Outline each Plasmodium falciparum-infected red blood cell.
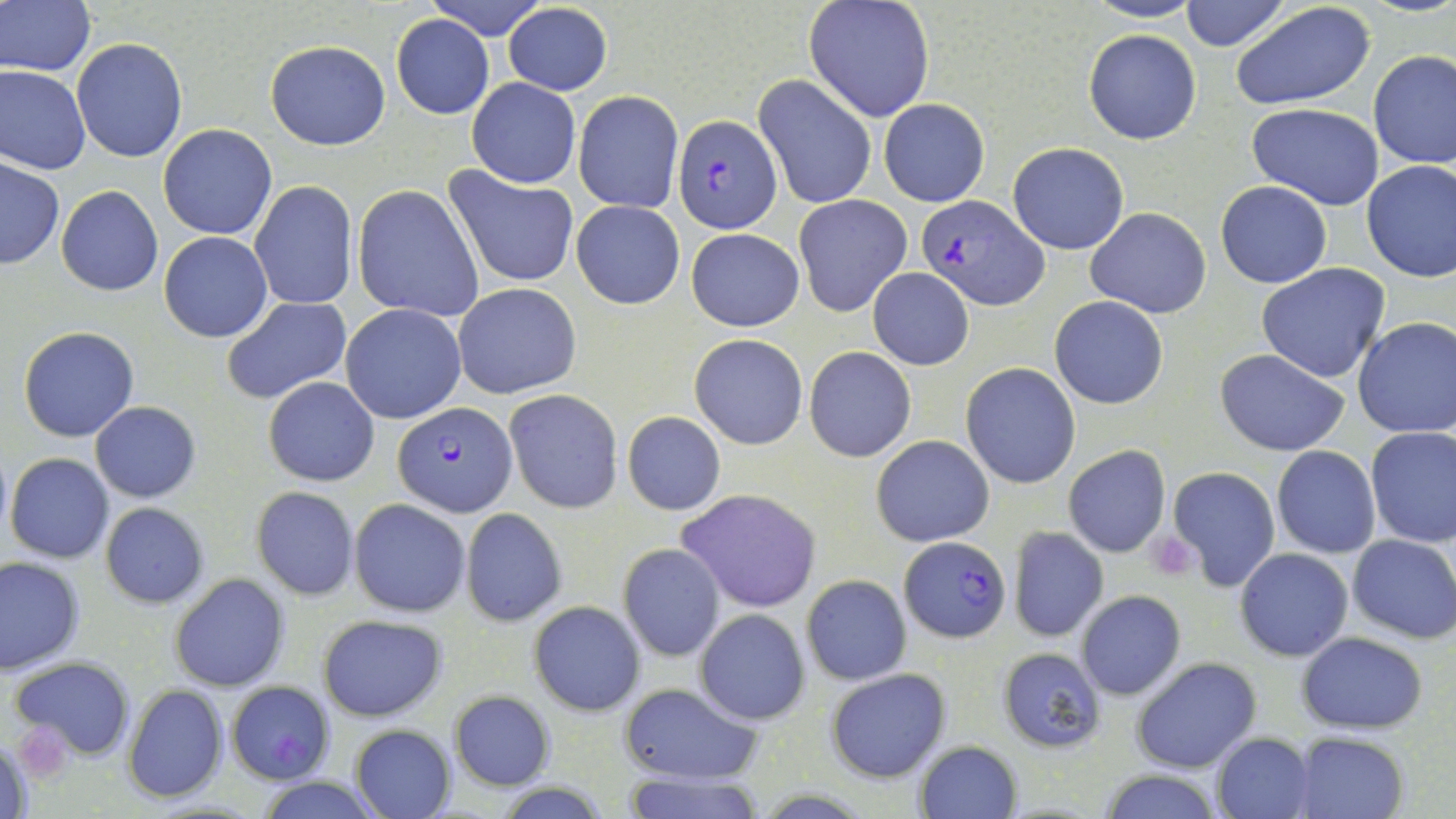
Approximate bounding boxes as [x1, y1, x2, y2] in pixels.
Plasmodium falciparum-infected red blood cells: [672, 114, 782, 233], [915, 195, 1050, 311], [392, 402, 516, 516], [897, 540, 1012, 644], [22, 725, 70, 783].

{
  "slide_level_diagnosis": "Plasmodium falciparum",
  "uninfected_red_blood_cell_locations": "approximate bounding boxes as [x1, y1, x2, y2] in pixels: [423, 0, 550, 41], [1085, 0, 1203, 24], [1181, 0, 1289, 51], [2, 1, 95, 77], [803, 1, 937, 122], [1231, 1, 1378, 110], [501, 3, 614, 95], [391, 15, 494, 120], [1084, 28, 1201, 144], [71, 37, 188, 163], [264, 40, 392, 150], [1368, 49, 1456, 169], [0, 64, 91, 175], [754, 74, 877, 208], [465, 77, 580, 189], [573, 91, 682, 213], [879, 100, 989, 206], [1247, 102, 1385, 211], [157, 124, 278, 240], [1007, 140, 1129, 254], [1, 158, 64, 269], [1360, 159, 1456, 282], [446, 166, 579, 288], [1215, 180, 1332, 288], [247, 182, 358, 309], [353, 184, 485, 322], [57, 186, 164, 296], [793, 194, 912, 316], [571, 199, 685, 310], [1085, 208, 1211, 318], [686, 227, 804, 332], [158, 231, 273, 342], [1256, 263, 1391, 384], [867, 268, 975, 371], [452, 282, 581, 400], [1050, 295, 1168, 410], [221, 296, 352, 404], [340, 303, 467, 424], [1352, 316, 1456, 438], [18, 327, 139, 443], [689, 333, 809, 451], [803, 347, 917, 462], [1214, 348, 1352, 457], [960, 363, 1081, 489], [263, 376, 381, 487], [504, 389, 623, 513], [91, 401, 201, 502], [622, 411, 726, 516], [1364, 427, 1456, 548], [871, 434, 994, 547], [1062, 444, 1171, 559], [1272, 445, 1381, 559], [5, 453, 115, 564], [1167, 466, 1280, 591], [252, 486, 359, 601], [676, 489, 823, 612], [349, 499, 470, 616], [99, 503, 209, 608], [459, 507, 567, 628], [1009, 526, 1108, 642], [1346, 534, 1456, 644], [617, 542, 727, 662], [1235, 548, 1354, 661], [0, 556, 84, 674], [170, 574, 289, 692], [801, 574, 911, 684], [1075, 590, 1186, 701], [529, 600, 645, 715], [695, 608, 810, 724], [318, 613, 447, 721], [1298, 631, 1429, 735], [996, 646, 1107, 753], [10, 656, 133, 761], [1131, 656, 1262, 773], [825, 669, 951, 782], [225, 680, 335, 784], [616, 681, 764, 785], [123, 684, 228, 803], [449, 691, 556, 790], [350, 723, 456, 817], [1211, 733, 1315, 819], [1296, 733, 1410, 819], [1, 735, 35, 819], [914, 739, 1021, 818], [622, 767, 768, 819], [1096, 767, 1226, 819], [253, 775, 383, 818]",
  "magnification": "1000x",
  "image_size": "1456×819 pixels",
  "preparation": "thin blood film",
  "platelet_locations": "approximate bounding boxes as [x1, y1, x2, y2] in pixels: [1146, 530, 1198, 578]",
  "field_of_view": "single",
  "stain": "May-Grünwald-Giemsa",
  "modality": "optical microscopy"
}